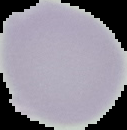

Summary:
  - Preparation: thin blood film
  - Result: no Plasmodium parasites seen
  - Image type: segmented cell region with the area outside set to black
  - Image size: 127×130 pixels